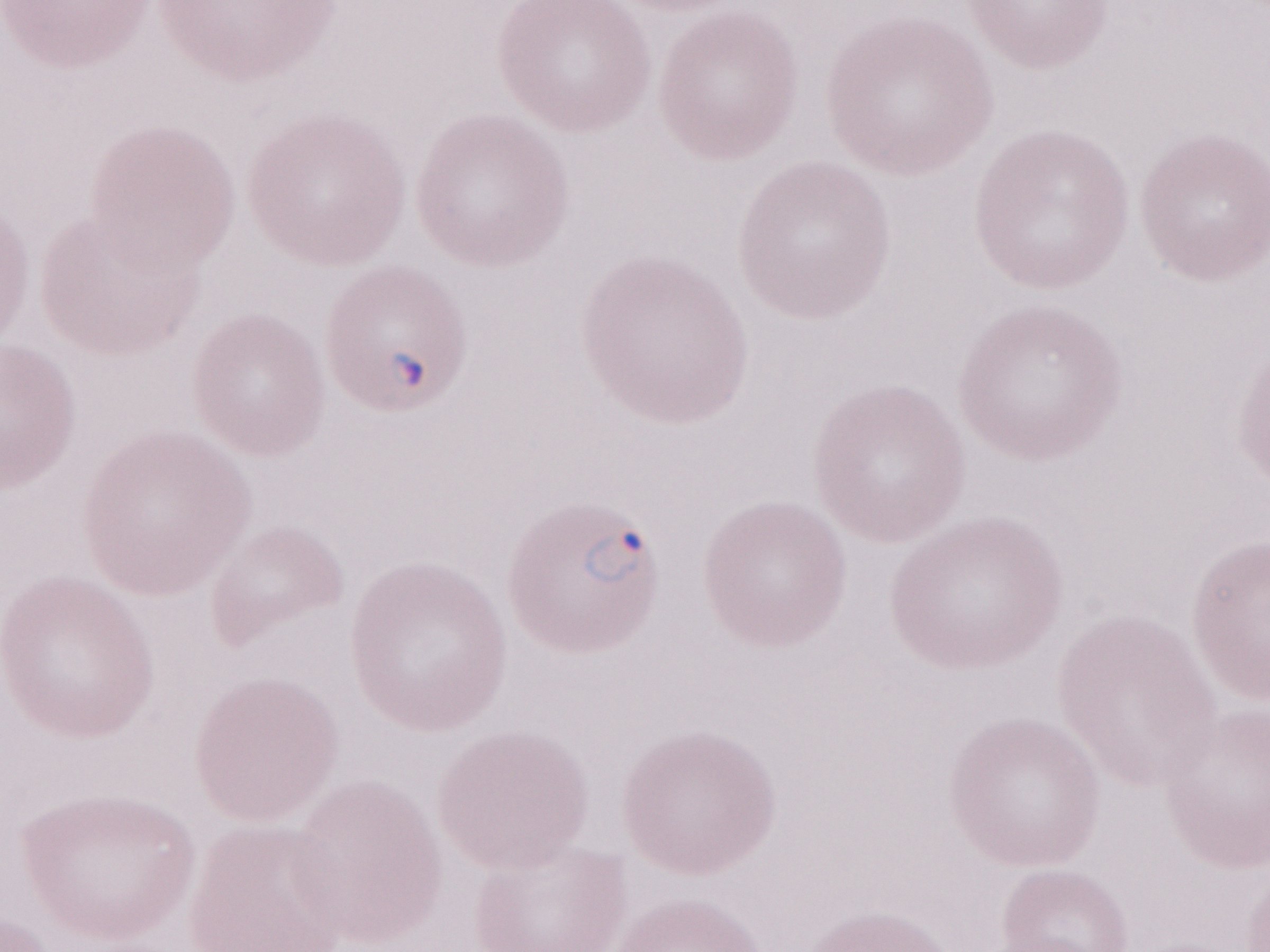

1,000x magnification. Single field of view. Olympus BX43 microscope and DP73 digital camera. May-Grünwald-Giemsa-stained preparation. Thin peripheral-blood smear. Malaria diagnosis (patient-level): positive. Image is 1270×952 pixels.